Identify the cell.
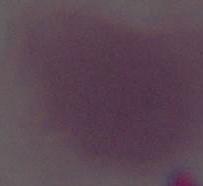

This is an erythrocyte.

Summary:
  - Modality: photomicrograph
  - Magnification: 1000x